Assess the morphology of the red blood cells.
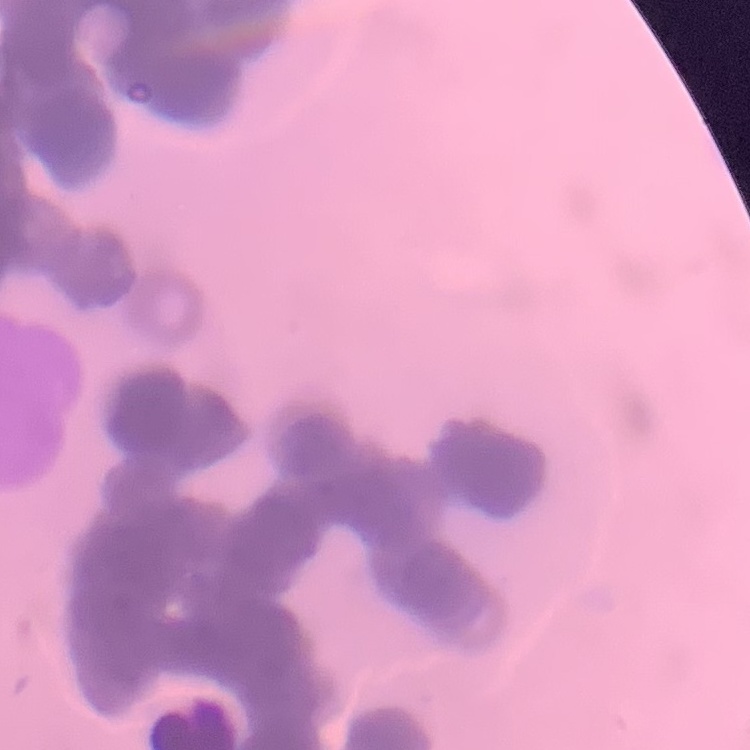
They show rouleaux formation.

One tile cut from a larger photomicrograph. Stained with either Field's or Giemsa. Thin blood film.